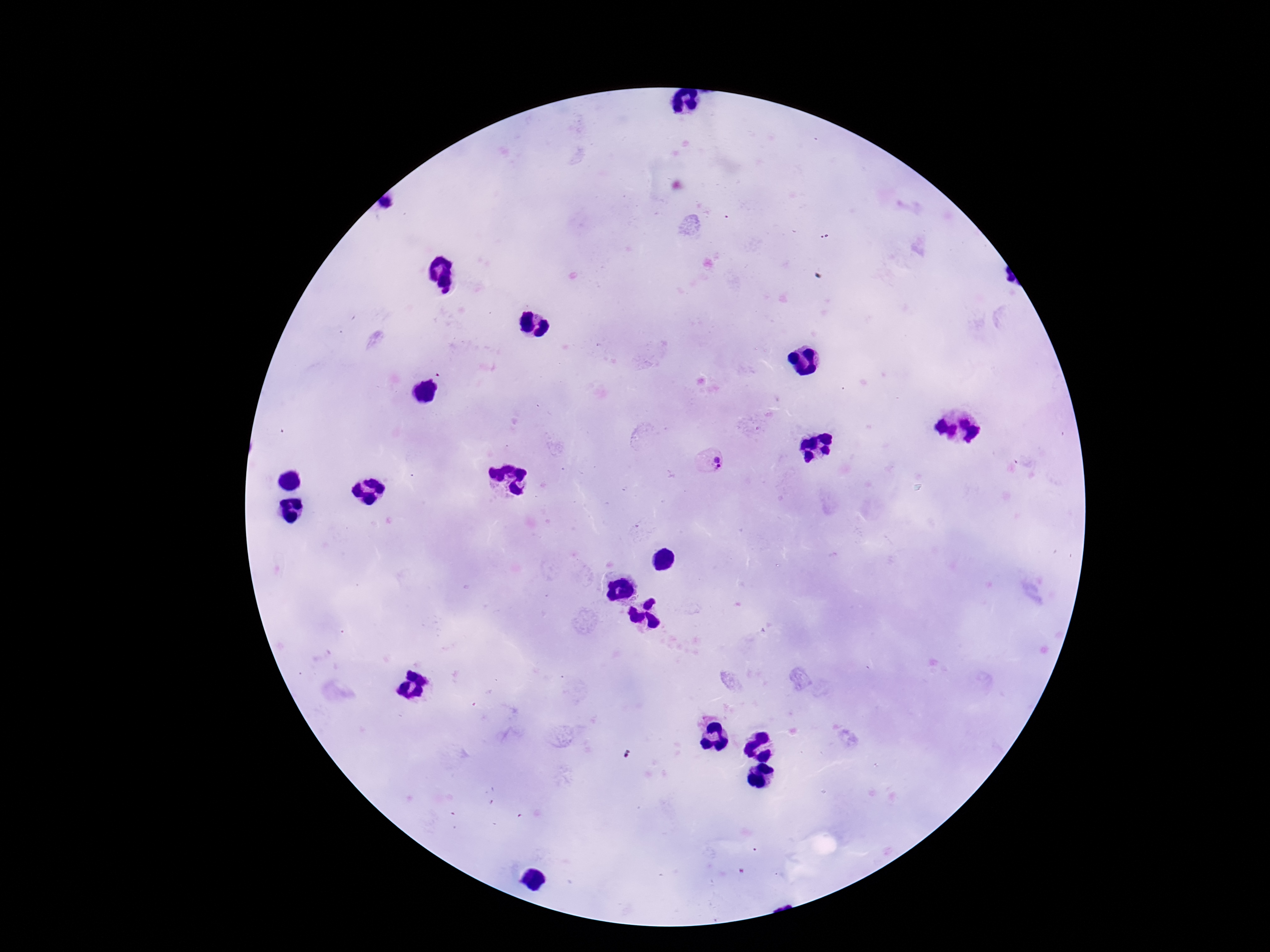 Approximate centers as [x, y] in pixels. Plasmodium parasite locations: [387, 202], [719, 462]. Smartphone photograph taken through the microscope eyepiece. One field from this slide. Giemsa-stained preparation. Patient malaria status: positive. Thick peripheral-blood smear. 100x magnification. Image is 1270×952 pixels.